Classify the preparation.
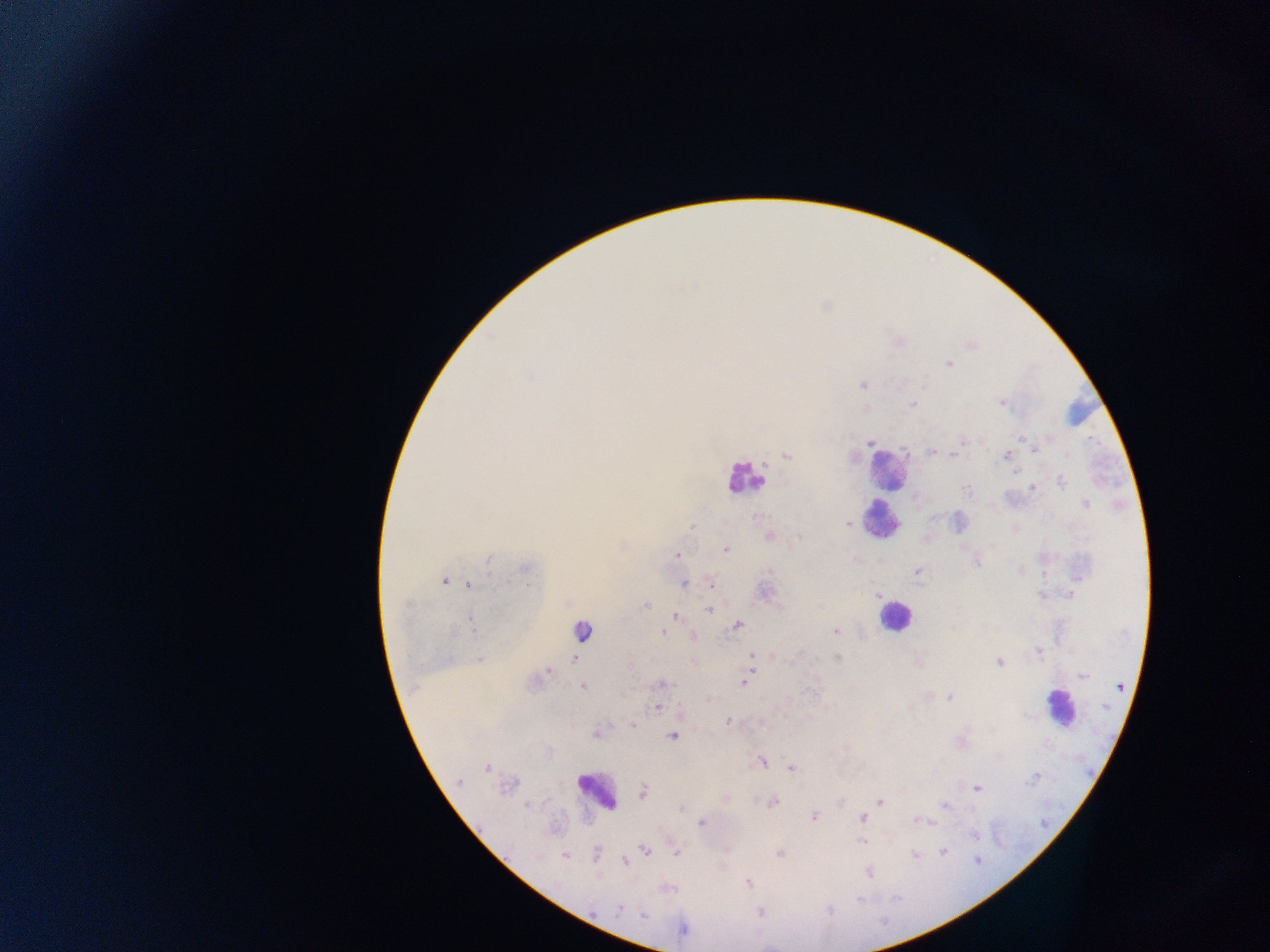
Thick blood film.

malaria_parasite_locations: 'approximate centers as {x, y} in pixels: {971, 347}, {948, 363}, {1001, 402}, {1049, 437}, {1022, 439}, {869, 443}, {930, 451}, {1034, 451}, {786, 456}, {954, 456}, {1004, 456}, {1068, 456}, {1016, 474}, {1060, 481}, {1034, 487}, {967, 491}, {1085, 504}, {848, 524}, {693, 527}, {725, 549}, {676, 555}, {488, 559}, {978, 563}, {917, 571}, {1044, 572}, {445, 581}, {710, 582}, {684, 584}, {468, 585}, {1070, 595}, {1043, 597}, {645, 606}, {709, 609}, {674, 615}, {738, 624}, {835, 631}, {661, 632}, {693, 634}, {1039, 652}, {752, 654}, {837, 657}, {479, 659}, {575, 660}, {548, 671}, {750, 674}, {660, 685}, {583, 687}, {949, 697}, {657, 709}, {727, 720}, {631, 726}, {595, 734}, {673, 738}, {763, 762}, {791, 767}, {487, 768}, {1037, 777}, {459, 782}, {976, 788}, {644, 794}, {774, 802}, {879, 802}, {527, 805}, {946, 807}, {814, 816}, {862, 818}, {702, 821}, {919, 822}, {930, 822}, {974, 836}, {861, 841}, {645, 849}, {678, 852}, {595, 854}, {942, 854}, {564, 856}, {623, 861}, {976, 862}, {869, 874}, {749, 882}, {895, 899}, {859, 901}, {622, 908}, {830, 910}, {760, 913}, {884, 920}'
capture: mobile-phone photograph through a microscope
field_of_view: single
country: Ghana
image_size: 1270×952 pixels
leukocyte_locations: 'approximate centers as {x, y} in pixels: {894, 618}, {1059, 707}, {596, 796}'